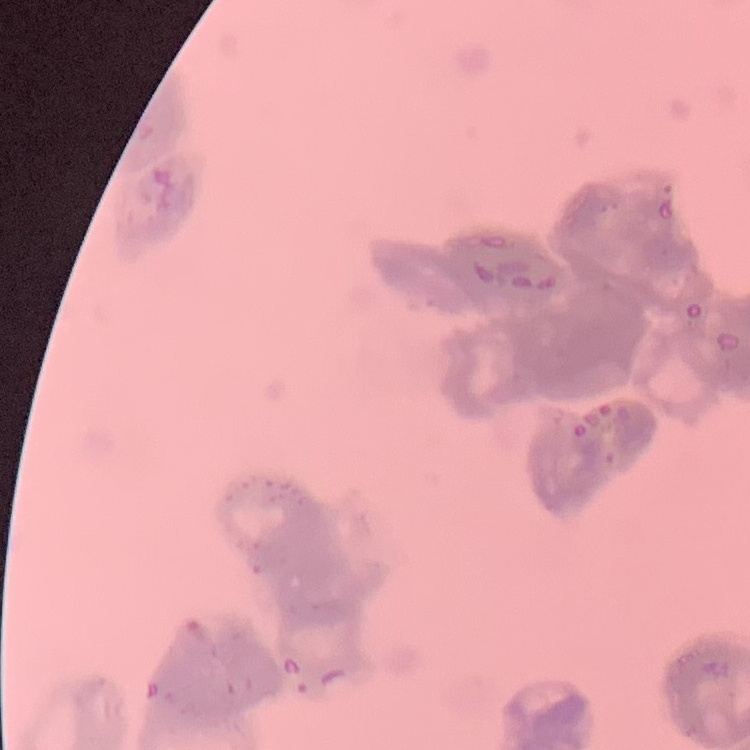

The red blood cells show rouleaux formation. Stained with either Field's or Giemsa. Thin blood smear. One tile cut from a larger photomicrograph.